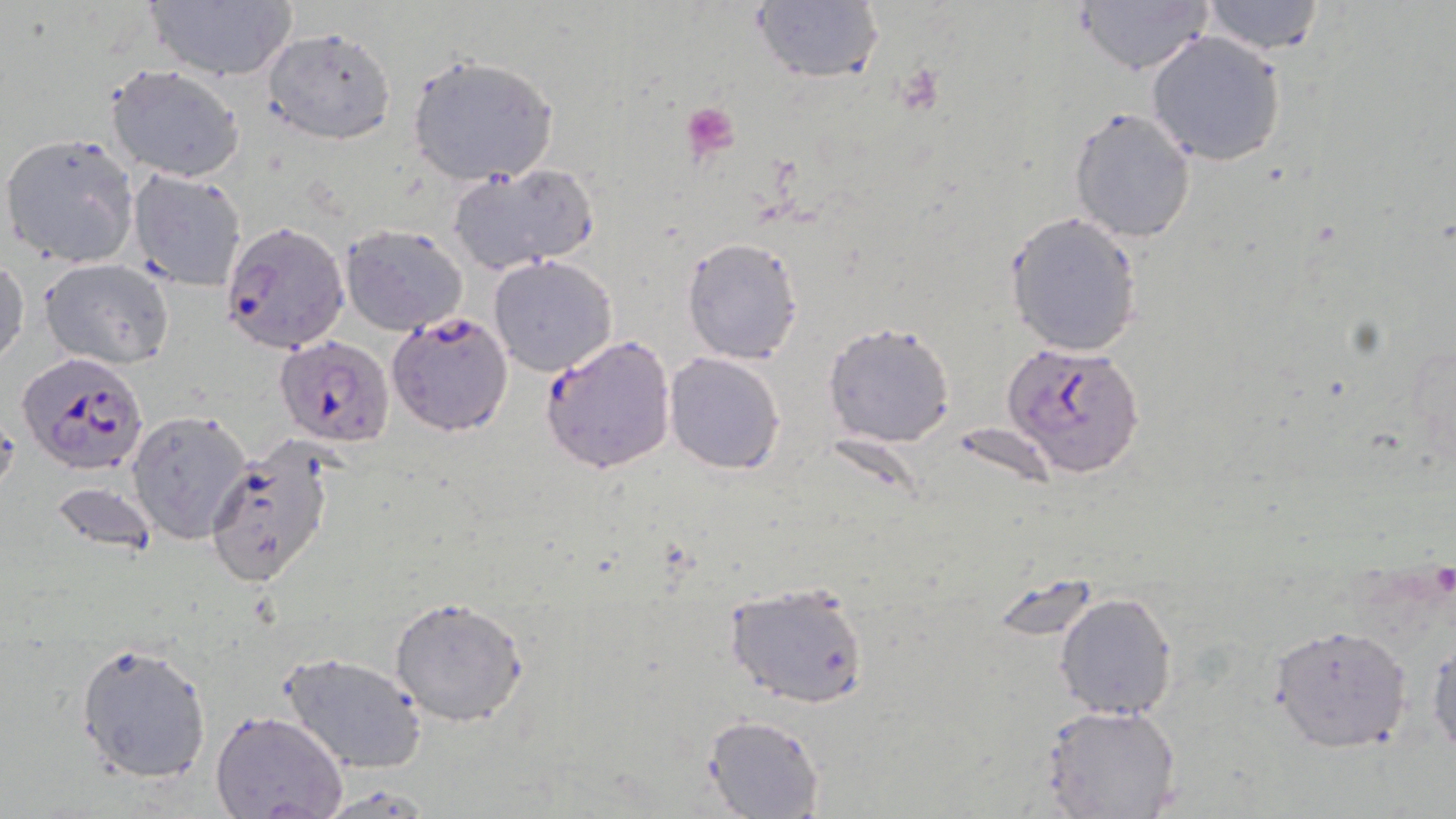
Approximate bounding boxes as (x1,y1)-(x2,y2) corner pairs in pixels. Uninfected red blood cell locations: (144,0)-(298,83), (1074,0)-(1216,74), (1200,0)-(1326,56), (748,2)-(884,85), (262,27)-(396,144), (1146,31)-(1286,167), (406,51)-(560,186), (105,64)-(246,184), (1068,106)-(1197,243), (3,131)-(139,269), (448,162)-(597,276), (128,169)-(247,290), (1004,211)-(1145,357), (341,222)-(470,336), (681,237)-(803,364), (1,255)-(27,367), (488,255)-(618,375), (39,257)-(175,369), (824,320)-(956,448), (663,352)-(786,476), (127,409)-(253,544), (725,579)-(870,710), (1054,591)-(1179,722), (389,596)-(529,726), (1269,624)-(1412,753), (1427,636)-(1456,756), (74,638)-(213,785), (281,651)-(426,773), (1039,705)-(1182,819), (209,711)-(349,819), (702,715)-(824,819). Platelet locations: (682,103)-(741,158). Plasmodium falciparum-infected red blood cell locations: (220,219)-(350,355), (386,311)-(514,436), (539,333)-(678,473), (276,336)-(394,447), (1001,341)-(1145,478), (18,351)-(149,477), (204,443)-(338,590). Slide-level diagnosis: Plasmodium falciparum. Image is 1456×819 pixels. Optical microscopy. May-Grünwald-Giemsa-stained preparation. One field of a larger specimen. 1000x magnification. Thin blood smear.